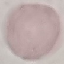

Result: no malaria parasites detected. Giemsa stain. Thin blood smear. Acquired by smartphone through the microscope eyepiece. Automatically extracted cell patch, resized to 64 × 64 pixels.